State which parasite is depicted.
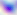
This is Toxoplasma gondii.

{
  "modality": "micrograph",
  "magnification": "400x"
}